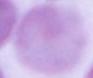
An erythrocyte is shown. Photomicrograph. Captured at 1000x magnification.